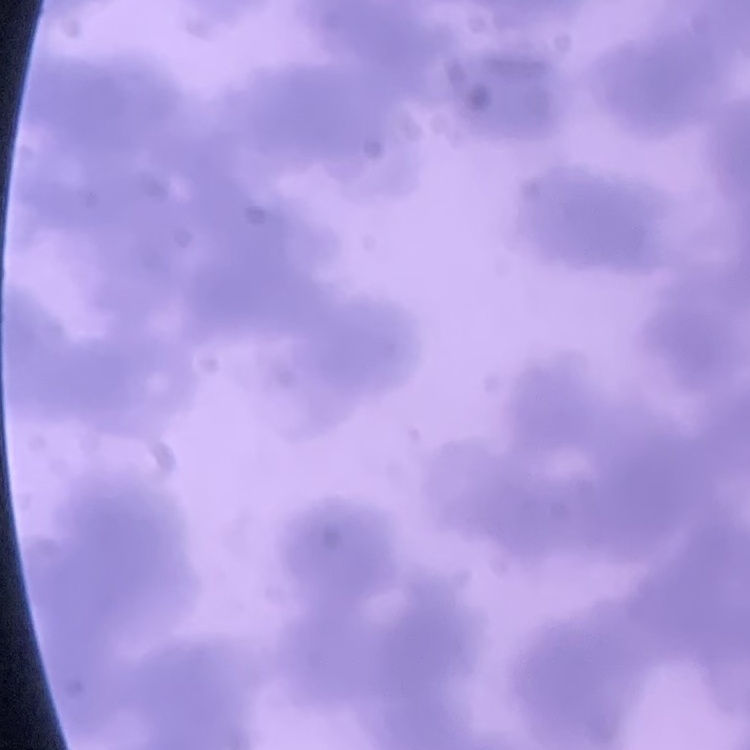 The red blood cells show rouleaux formation. Field's or Giemsa stain. Thin peripheral smear. One tile cut from a larger photomicrograph.